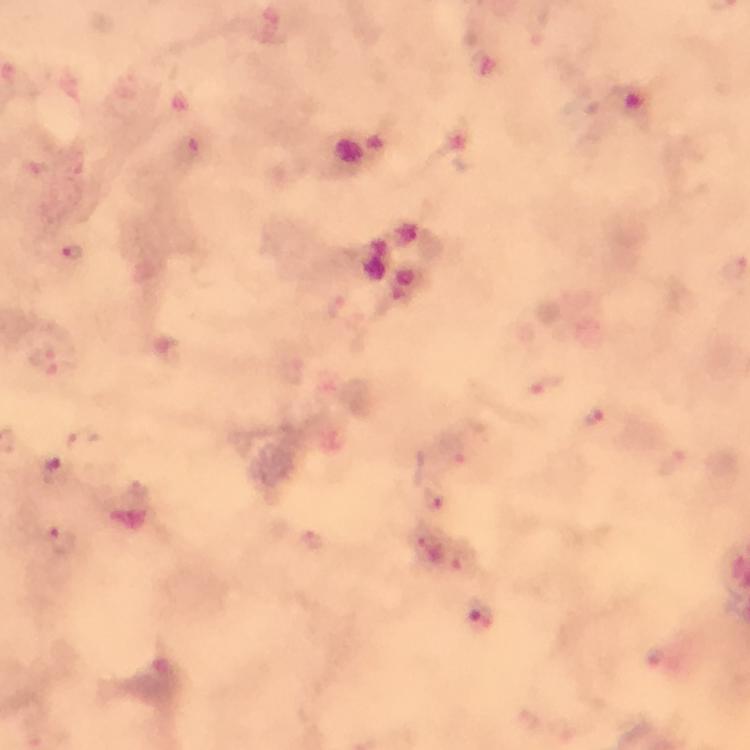
Approximate centers as [x, y] in pixels. Malaria parasite locations: [190, 148], [73, 253], [47, 360], [542, 385], [595, 417], [455, 452], [674, 462], [57, 470], [436, 501], [62, 541], [313, 542], [429, 548], [462, 564], [482, 614]. Image is 750×750 pixels. Cropped region of a single field of view. Thick smear. Giemsa-stained preparation. At 100x magnification. Immersion oil applied. Photographed with a smartphone mounted on the microscope. From a diagnostic examination for malaria.